Assess the morphology of the red blood cells.
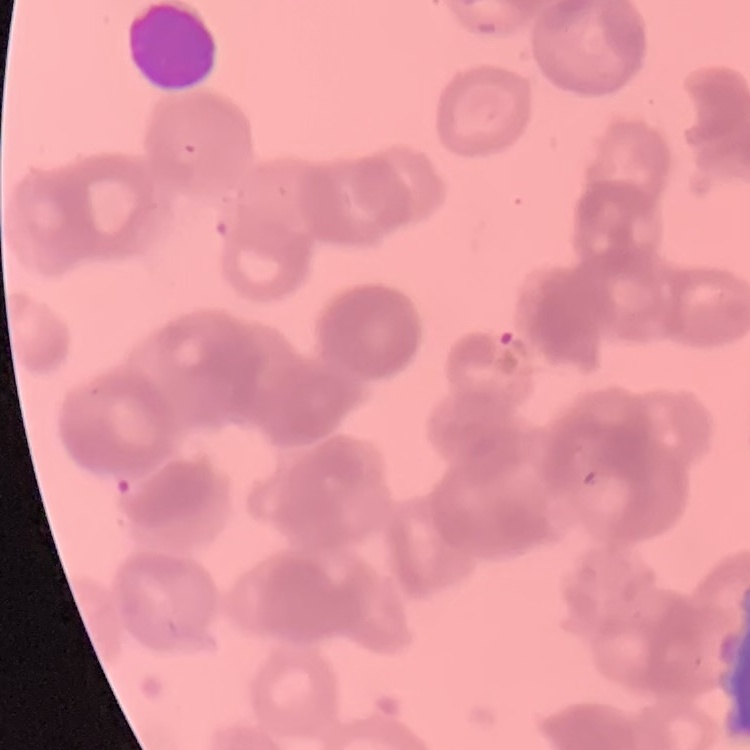
They show rouleaux formation.

One tile cut from a larger photomicrograph. Thin blood film. Field's or Giemsa stain.